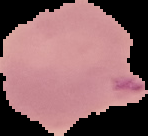 From a thin blood film. Malaria status: parasitized. Image is 148×136 pixels. Segmented cell region on a black background.